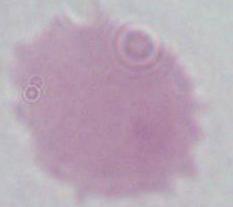
Summary:
  - Magnification: 1000x
  - Identification: erythrocyte
  - Modality: micrograph